Locate and identify every blood parasite.
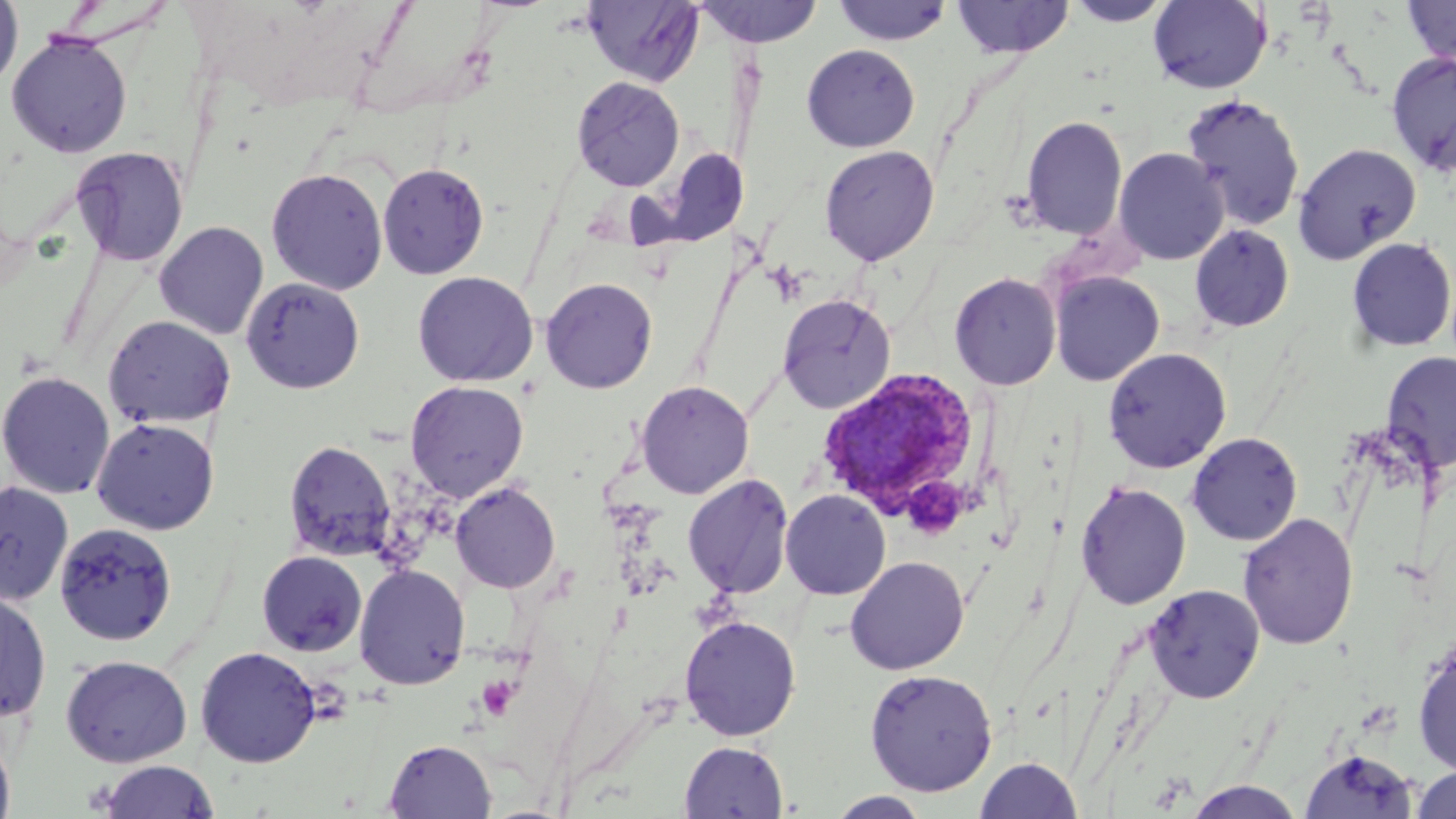

Approximate bounding boxes as named x1/y1/x2/y2 corners in pixels.
Plasmodium vivax-infected red blood cells: (x1=815, y1=366, x2=989, y2=528).
No Plasmodium falciparum, Plasmodium ovale, Plasmodium malariae, Babesia divergens, or Trypanosoma brucei observed.

Uninfected red blood cell locations: (x1=0, y1=0, x2=23, y2=93), (x1=582, y1=0, x2=704, y2=87), (x1=693, y1=0, x2=825, y2=48), (x1=951, y1=0, x2=1075, y2=58), (x1=1401, y1=0, x2=1456, y2=67), (x1=831, y1=1, x2=954, y2=46), (x1=1063, y1=1, x2=1174, y2=26), (x1=1148, y1=1, x2=1272, y2=93), (x1=6, y1=33, x2=132, y2=158), (x1=801, y1=44, x2=920, y2=152), (x1=1386, y1=52, x2=1456, y2=175), (x1=571, y1=77, x2=685, y2=191), (x1=1180, y1=93, x2=1305, y2=231), (x1=1021, y1=115, x2=1128, y2=241), (x1=1292, y1=142, x2=1421, y2=265), (x1=820, y1=145, x2=939, y2=265), (x1=645, y1=146, x2=745, y2=248), (x1=71, y1=147, x2=190, y2=267), (x1=1114, y1=147, x2=1228, y2=265), (x1=377, y1=162, x2=489, y2=279), (x1=266, y1=167, x2=388, y2=294), (x1=154, y1=221, x2=269, y2=340), (x1=1189, y1=224, x2=1295, y2=333), (x1=1346, y1=237, x2=1456, y2=353), (x1=1049, y1=270, x2=1164, y2=386), (x1=412, y1=271, x2=539, y2=388), (x1=949, y1=272, x2=1061, y2=390), (x1=241, y1=277, x2=365, y2=394), (x1=540, y1=277, x2=658, y2=394), (x1=777, y1=293, x2=896, y2=414), (x1=102, y1=314, x2=236, y2=429), (x1=1103, y1=347, x2=1231, y2=473), (x1=1380, y1=349, x2=1455, y2=472), (x1=0, y1=370, x2=116, y2=499), (x1=405, y1=380, x2=528, y2=502), (x1=636, y1=380, x2=754, y2=499), (x1=91, y1=417, x2=220, y2=535), (x1=1186, y1=431, x2=1302, y2=545), (x1=283, y1=439, x2=397, y2=562), (x1=682, y1=474, x2=795, y2=599), (x1=0, y1=480, x2=74, y2=607), (x1=450, y1=481, x2=561, y2=594), (x1=1075, y1=481, x2=1192, y2=610), (x1=780, y1=489, x2=890, y2=600), (x1=1237, y1=512, x2=1358, y2=650), (x1=54, y1=522, x2=178, y2=647), (x1=257, y1=550, x2=367, y2=656), (x1=845, y1=556, x2=969, y2=675), (x1=354, y1=564, x2=470, y2=690), (x1=1145, y1=584, x2=1265, y2=703), (x1=0, y1=587, x2=52, y2=725), (x1=679, y1=615, x2=801, y2=741), (x1=1412, y1=642, x2=1456, y2=777), (x1=194, y1=645, x2=322, y2=767), (x1=60, y1=654, x2=193, y2=767), (x1=864, y1=668, x2=998, y2=796), (x1=0, y1=731, x2=16, y2=819), (x1=383, y1=739, x2=496, y2=818), (x1=679, y1=741, x2=788, y2=819), (x1=1299, y1=748, x2=1418, y2=819), (x1=974, y1=757, x2=1083, y2=818), (x1=96, y1=760, x2=221, y2=819), (x1=1411, y1=766, x2=1456, y2=819), (x1=1185, y1=780, x2=1304, y2=818), (x1=827, y1=791, x2=931, y2=818). Slide-level diagnosis: Plasmodium vivax. Optical microscopy. Thin blood film. May-Grünwald-Giemsa stain. Image is 1456×819 pixels. Single field of view. 1000x magnification.